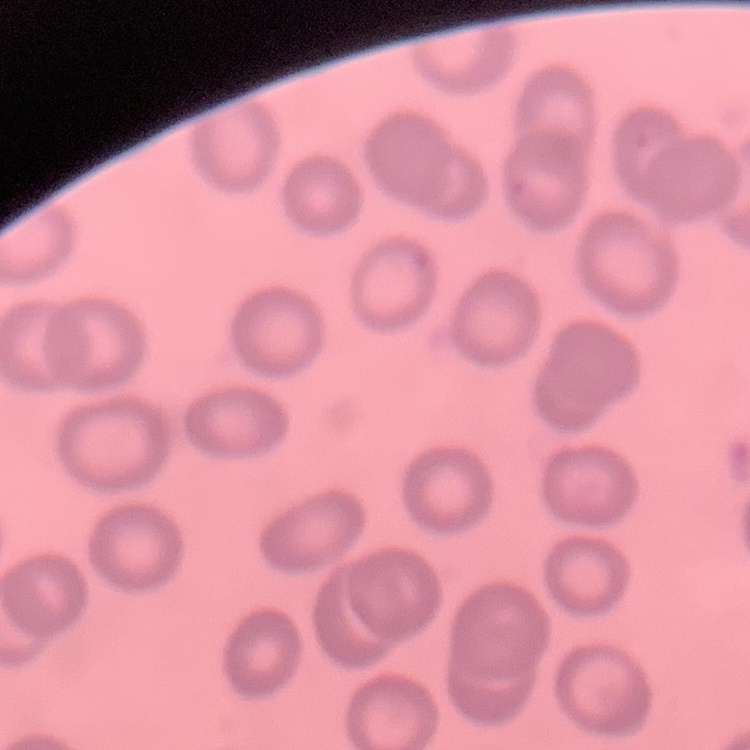

Summary:
  - Red blood cell morphology: no rouleaux formation
  - Stain: Field's or Giemsa
  - Preparation: thin peripheral smear
  - Image type: square crop of a larger photomicrograph